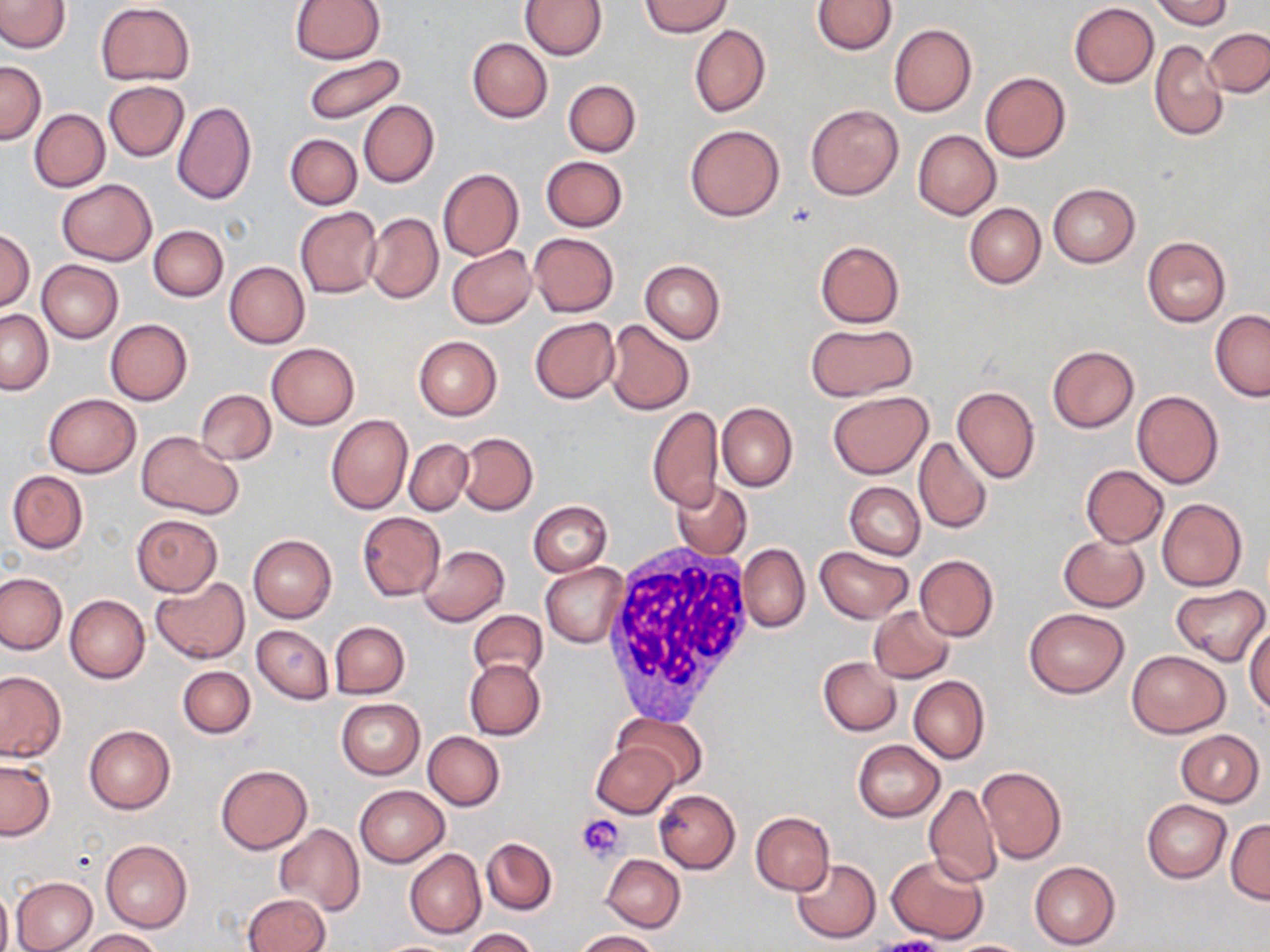

{
  "slide_level_diagnosis": "no evidence of blood parasites",
  "stain": "May-Grünwald-Giemsa",
  "magnification": "1000x",
  "image_size": "1270×952 pixels",
  "modality": "optical microscopy",
  "uninfected_red_blood_cell_locations": "approximate bounding boxes as (x1,y1)-(x2,y2) corner pairs in pixels: (0,0)-(70,53), (290,0)-(384,63), (640,0)-(732,38), (812,0)-(895,55), (1153,0)-(1232,28), (520,1)-(606,59), (95,2)-(194,86), (1069,2)-(1159,87), (689,23)-(770,119), (889,23)-(976,117), (1204,29)-(1269,98), (467,38)-(552,122), (1150,38)-(1227,141), (302,53)-(408,126), (0,60)-(45,143), (981,72)-(1071,162), (556,79)-(635,231), (563,80)-(640,156), (104,81)-(189,162), (172,100)-(257,206), (358,100)-(439,188), (805,105)-(903,201), (30,109)-(109,191), (685,125)-(784,221), (913,130)-(1001,219), (285,133)-(361,209), (541,156)-(627,232), (438,168)-(524,261), (56,179)-(157,264), (1048,183)-(1139,267), (964,203)-(1045,288), (295,207)-(382,298), (364,213)-(443,304), (148,225)-(228,302), (0,229)-(34,310), (529,232)-(618,317), (1142,237)-(1231,327), (816,240)-(905,327), (447,245)-(537,327), (37,259)-(123,342), (640,259)-(725,343), (224,261)-(309,349), (1,310)-(53,394), (1210,310)-(1270,401), (530,317)-(619,404), (104,318)-(192,405), (603,320)-(695,415), (806,323)-(916,401), (413,336)-(502,420), (267,342)-(360,429), (1047,345)-(1138,433), (952,386)-(1039,484), (195,388)-(276,465), (827,391)-(933,479), (1132,391)-(1224,489), (43,394)-(141,477), (717,402)-(797,493), (647,407)-(723,512), (326,415)-(413,515), (137,432)-(241,517), (457,432)-(538,516), (914,436)-(992,534), (405,439)-(473,515), (1081,466)-(1168,547), (7,470)-(88,553), (671,480)-(751,560), (845,482)-(924,559), (1156,497)-(1248,592), (528,500)-(612,577), (357,511)-(445,601), (132,514)-(222,595), (247,533)-(336,623), (1058,535)-(1150,611), (738,544)-(810,633), (419,545)-(510,626), (815,546)-(913,623), (914,555)-(998,642), (541,562)-(628,647), (0,571)-(66,654), (150,577)-(249,663), (1170,584)-(1266,665), (65,594)-(149,683), (869,605)-(954,683), (1023,608)-(1130,698), (469,610)-(548,683), (328,621)-(410,699), (1246,621)-(1270,715), (252,625)-(333,703), (1126,650)-(1231,738), (819,656)-(901,736), (465,659)-(546,740), (178,666)-(255,738), (0,671)-(66,762), (909,675)-(989,764), (336,699)-(424,779), (613,712)-(708,790), (84,724)-(175,814), (1175,729)-(1263,807), (422,731)-(505,810), (852,740)-(945,822), (593,744)-(678,818), (0,759)-(55,840), (215,764)-(313,854), (977,766)-(1067,864), (924,783)-(1001,887), (354,785)-(448,868), (654,789)-(740,873), (1142,799)-(1231,883), (750,812)-(835,895), (1226,818)-(1269,903), (275,824)-(363,914), (482,837)-(558,915), (101,839)-(192,932), (406,848)-(485,938), (887,853)-(988,944), (602,854)-(685,932), (792,859)-(882,943), (1029,860)-(1121,949), (11,876)-(97,951), (0,881)-(12,952), (242,893)-(330,952), (462,928)-(540,952), (78,929)-(164,951), (576,930)-(659,951), (946,939)-(1034,951), (371,940)-(464,952)",
  "white_blood_cell_locations": "approximate bounding boxes as (x1,y1)-(x2,y2) corner pairs in pixels: (598,543)-(758,725)",
  "preparation": "thin blood film",
  "platelet_locations": "approximate bounding boxes as (x1,y1)-(x2,y2) corner pairs in pixels: (577,813)-(625,862)",
  "field_of_view": "single"
}